State the blood parasite species.
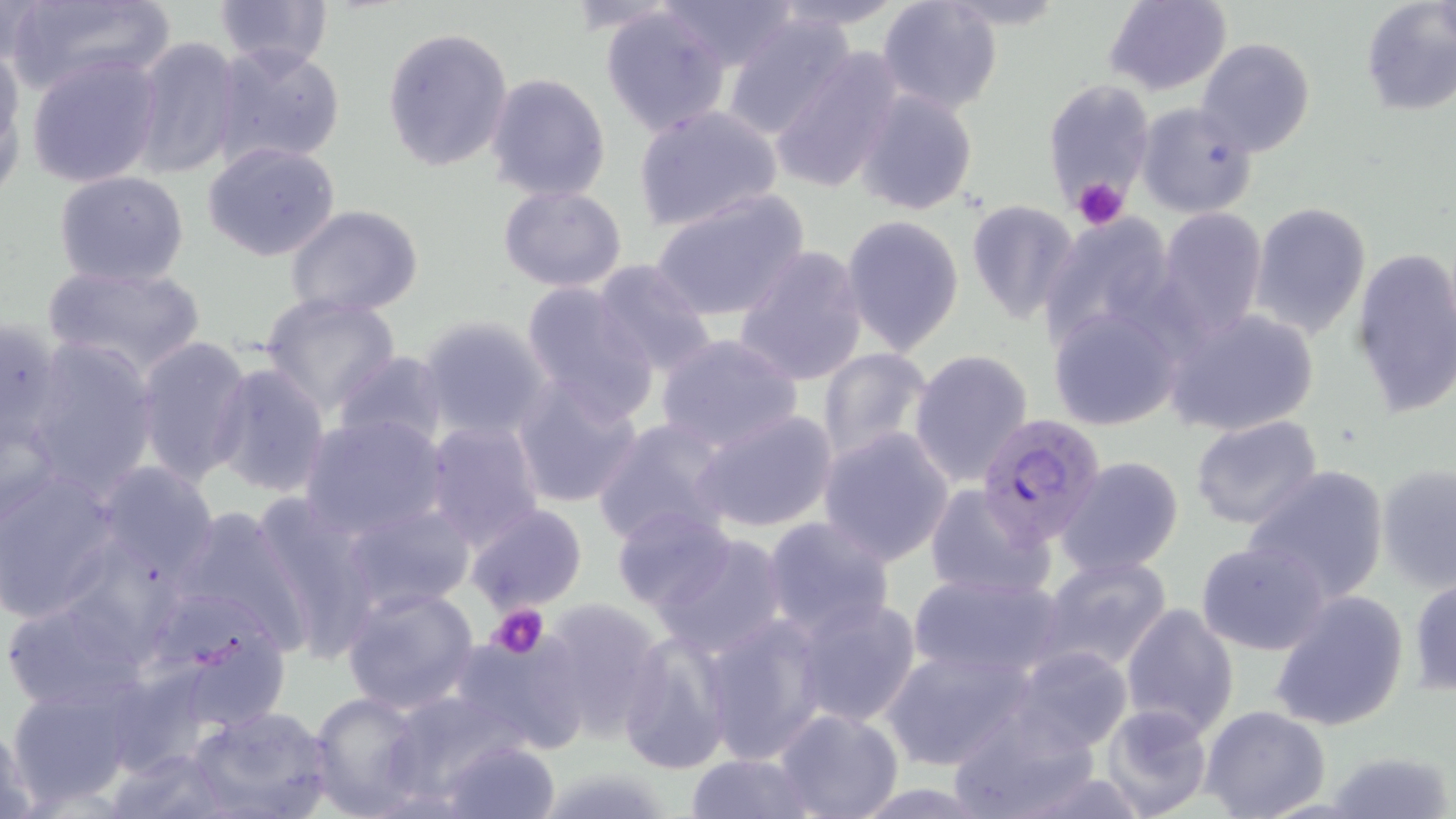

Plasmodium falciparum.

stain = May-Grünwald-Giemsa
field of view = one of a larger specimen
modality = light microscopy
Plasmodium falciparum-infected red blood cell locations = approximate bounding boxes as (x1,y1)-(x2,y2) corner pairs in pixels: (977,412)-(1110,544)
uninfected red blood cell locations = approximate bounding boxes as (x1,y1)-(x2,y2) corner pairs in pixels: (5,0)-(176,100), (213,0)-(333,72), (652,0)-(801,70), (766,0)-(909,33), (876,0)-(1004,115), (1102,0)-(1232,96), (1360,2)-(1456,116), (598,4)-(734,136), (720,11)-(860,141), (382,26)-(513,172), (129,35)-(244,182), (1196,37)-(1315,158), (210,42)-(347,168), (0,47)-(25,197), (27,52)-(163,188), (766,52)-(902,195), (485,73)-(612,201), (1041,76)-(1158,214), (855,88)-(979,216), (1134,101)-(1259,218), (633,106)-(783,231), (203,141)-(343,262), (53,171)-(189,288), (498,184)-(627,292), (650,187)-(809,322), (965,199)-(1080,323), (1248,202)-(1371,340), (285,205)-(424,315), (1158,208)-(1267,338), (1038,213)-(1180,349), (841,215)-(965,358), (732,244)-(870,388), (1349,247)-(1456,417), (590,260)-(720,379), (44,262)-(204,381), (520,280)-(660,422), (260,294)-(401,414), (1046,304)-(1184,432), (1163,308)-(1319,435), (416,315)-(554,439), (0,316)-(70,455), (655,333)-(803,453), (134,335)-(253,485), (20,339)-(160,497), (816,346)-(935,464), (908,349)-(1034,487), (332,350)-(451,456), (208,362)-(331,499), (510,375)-(645,510), (691,408)-(839,535), (298,413)-(449,540), (1189,416)-(1325,531), (591,417)-(738,550), (422,419)-(546,550), (817,427)-(955,565), (1056,456)-(1185,576), (90,460)-(219,584), (1243,464)-(1391,602), (1376,464)-(1456,591), (0,467)-(120,623), (925,483)-(1055,599), (248,494)-(381,654), (170,500)-(315,657), (340,502)-(478,614), (464,505)-(589,616), (612,507)-(739,615), (761,516)-(896,639), (649,531)-(794,660), (1196,541)-(1330,656), (1040,554)-(1174,673), (907,570)-(1068,680), (1409,577)-(1456,697), (339,585)-(482,716), (1268,590)-(1409,732), (0,593)-(156,714), (792,596)-(922,730), (537,597)-(667,741), (1120,602)-(1239,740), (698,614)-(829,764), (446,633)-(585,755), (617,633)-(732,775), (879,643)-(1035,771), (1007,646)-(1135,753), (5,685)-(134,808), (307,690)-(430,816), (384,690)-(530,802), (945,701)-(1104,819), (1098,702)-(1213,818), (1200,705)-(1331,819), (184,706)-(336,819), (773,707)-(905,819), (0,708)-(40,819), (439,740)-(558,819), (103,748)-(230,819), (1323,750)-(1456,819), (683,751)-(817,819)
magnification = 1000x
image size = 1456×819 pixels
platelet locations = approximate bounding boxes as (x1,y1)-(x2,y2) corner pairs in pixels: (1073,177)-(1130,230), (487,604)-(549,658)
preparation = thin blood smear